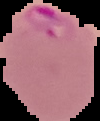

image type = cell region segmented out of the field of view; surrounding area masked to black
image size = 100×121 pixels
preparation = thin blood film
malaria status = parasitized